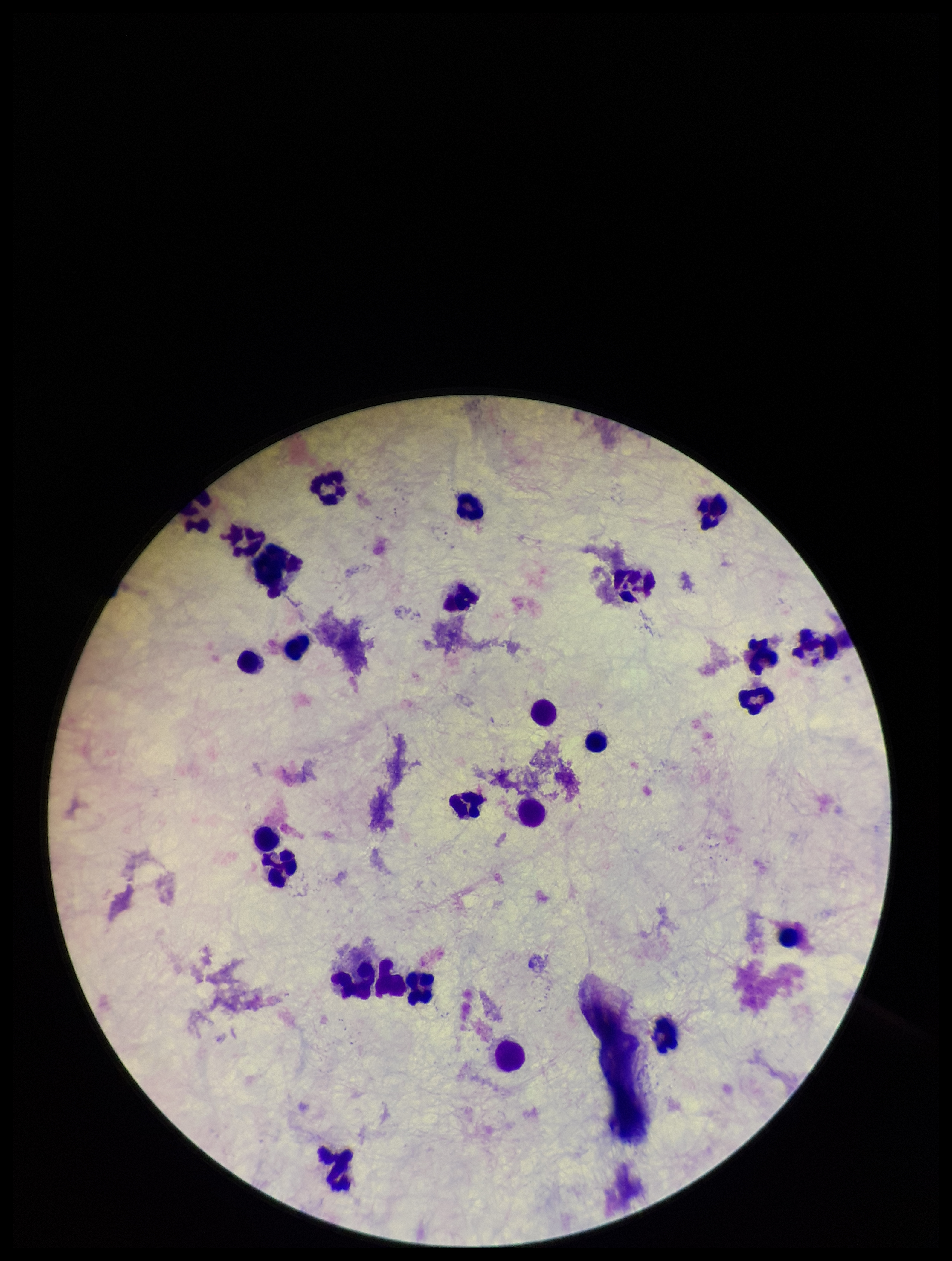
Summary:
  - Image size: 952×1261 pixels
  - Parasite count: 0
  - Field of view: single
  - Leukocyte count: 24
  - Patient malaria status: negative
  - Plasmodium parasites: none identified
  - Preparation: thick blood smear
  - Stain: Giemsa
  - Capture: smartphone photograph through the microscope eyepiece